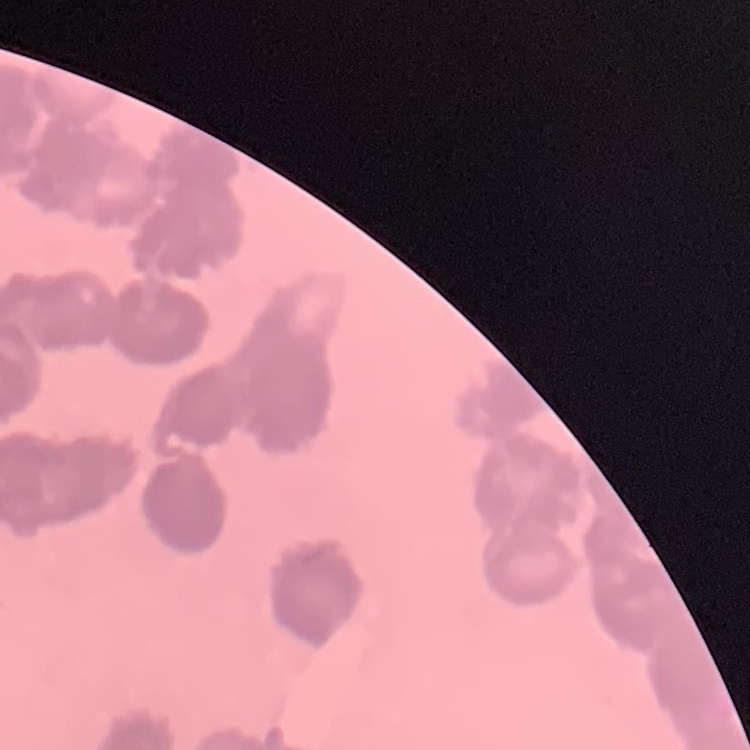 The erythrocytes exhibit rouleaux formation. Thin peripheral smear. Square crop of a larger photomicrograph. Field's or Giemsa stain.